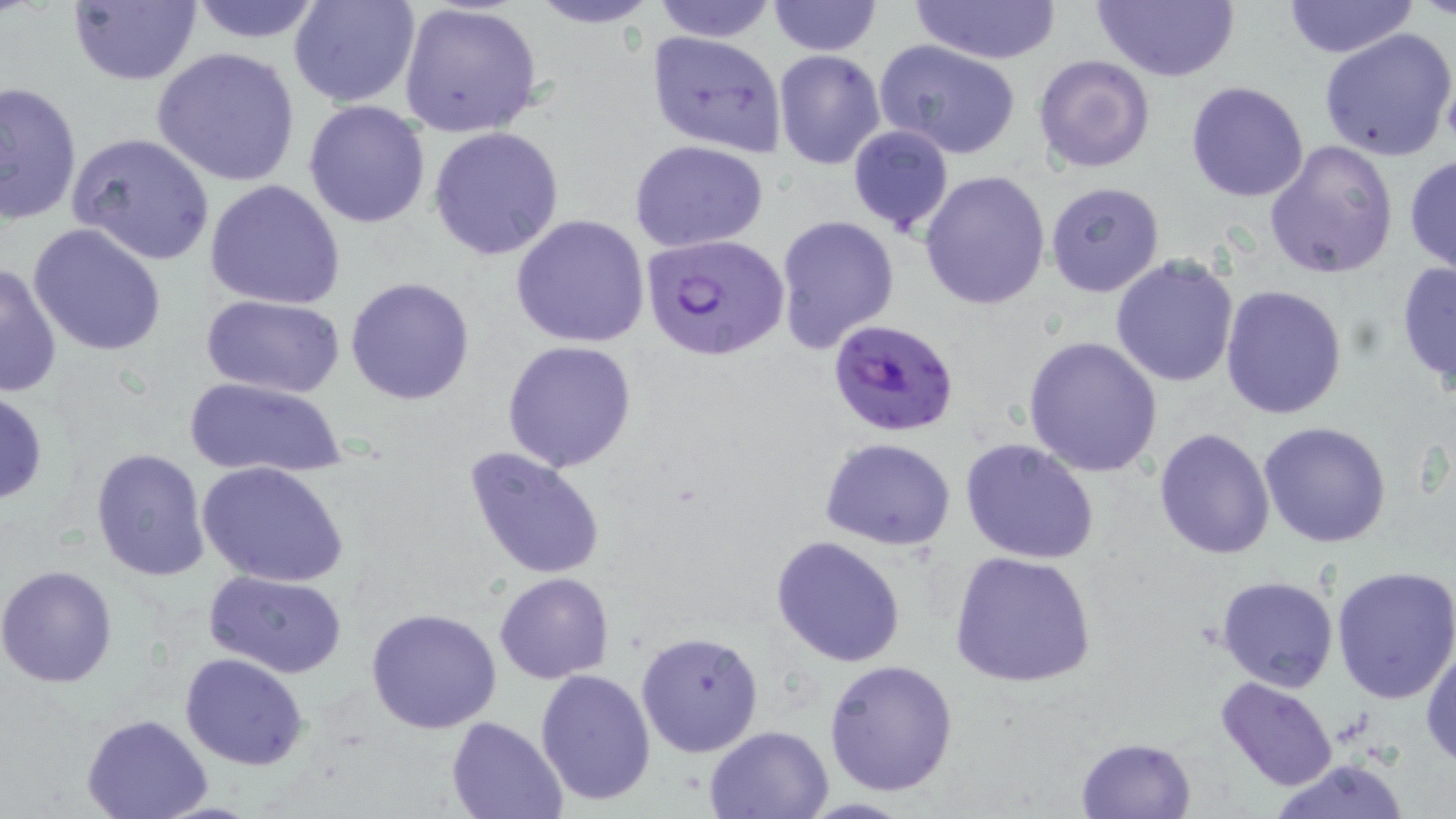

slide-level diagnosis = Plasmodium falciparum
preparation = thin blood film
modality = optical microscopy
Plasmodium falciparum-infected red blood cell locations = approximate bounding boxes as [x1, y1, x2, y2] in pixels: [641, 232, 791, 359], [829, 320, 960, 438]
uninfected red blood cell locations = approximate bounding boxes as [x1, y1, x2, y2] in pixels: [66, 0, 203, 87], [185, 0, 330, 45], [288, 0, 421, 110], [525, 0, 663, 28], [648, 0, 779, 43], [908, 0, 1063, 64], [1088, 0, 1242, 82], [399, 1, 544, 140], [766, 1, 882, 56], [1283, 1, 1419, 56], [1318, 28, 1456, 161], [645, 30, 786, 157], [874, 40, 1023, 160], [152, 46, 302, 188], [773, 50, 884, 170], [1032, 54, 1155, 173], [0, 81, 82, 225], [1186, 81, 1310, 202], [303, 100, 432, 229], [846, 123, 954, 237], [428, 125, 565, 260], [67, 131, 217, 267], [630, 140, 770, 252], [1264, 141, 1398, 280], [1403, 153, 1456, 276], [920, 169, 1050, 309], [205, 179, 346, 310], [1044, 180, 1164, 299], [509, 214, 652, 347], [775, 214, 900, 354], [26, 222, 169, 356], [1110, 255, 1240, 389], [1394, 259, 1456, 395], [1, 261, 63, 401], [345, 276, 476, 407], [1220, 285, 1348, 419], [203, 294, 345, 397], [1022, 335, 1163, 478], [501, 340, 636, 472], [182, 375, 348, 481], [0, 388, 49, 506], [1258, 421, 1393, 549], [1153, 426, 1275, 560], [821, 438, 955, 551], [960, 439, 1100, 566], [461, 444, 610, 581], [90, 447, 211, 582], [196, 460, 348, 589], [770, 534, 909, 667], [948, 550, 1098, 690], [1330, 565, 1456, 705], [0, 566, 117, 687], [205, 569, 349, 678], [495, 572, 615, 683], [1216, 575, 1339, 694], [366, 606, 503, 735], [636, 631, 763, 756], [1419, 635, 1456, 768], [180, 653, 309, 770], [825, 659, 958, 796], [534, 669, 657, 807], [1215, 676, 1340, 791], [82, 714, 212, 819], [444, 716, 567, 819], [704, 724, 837, 817], [1076, 736, 1196, 817], [1265, 759, 1415, 818]
field of view = one of a larger specimen
image size = 1456×819 pixels
stain = May-Grünwald-Giemsa
magnification = 1000x